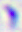 Photomicrograph. Toxoplasma gondii is seen. 400x magnification.